Outline each blood parasite and name the species.
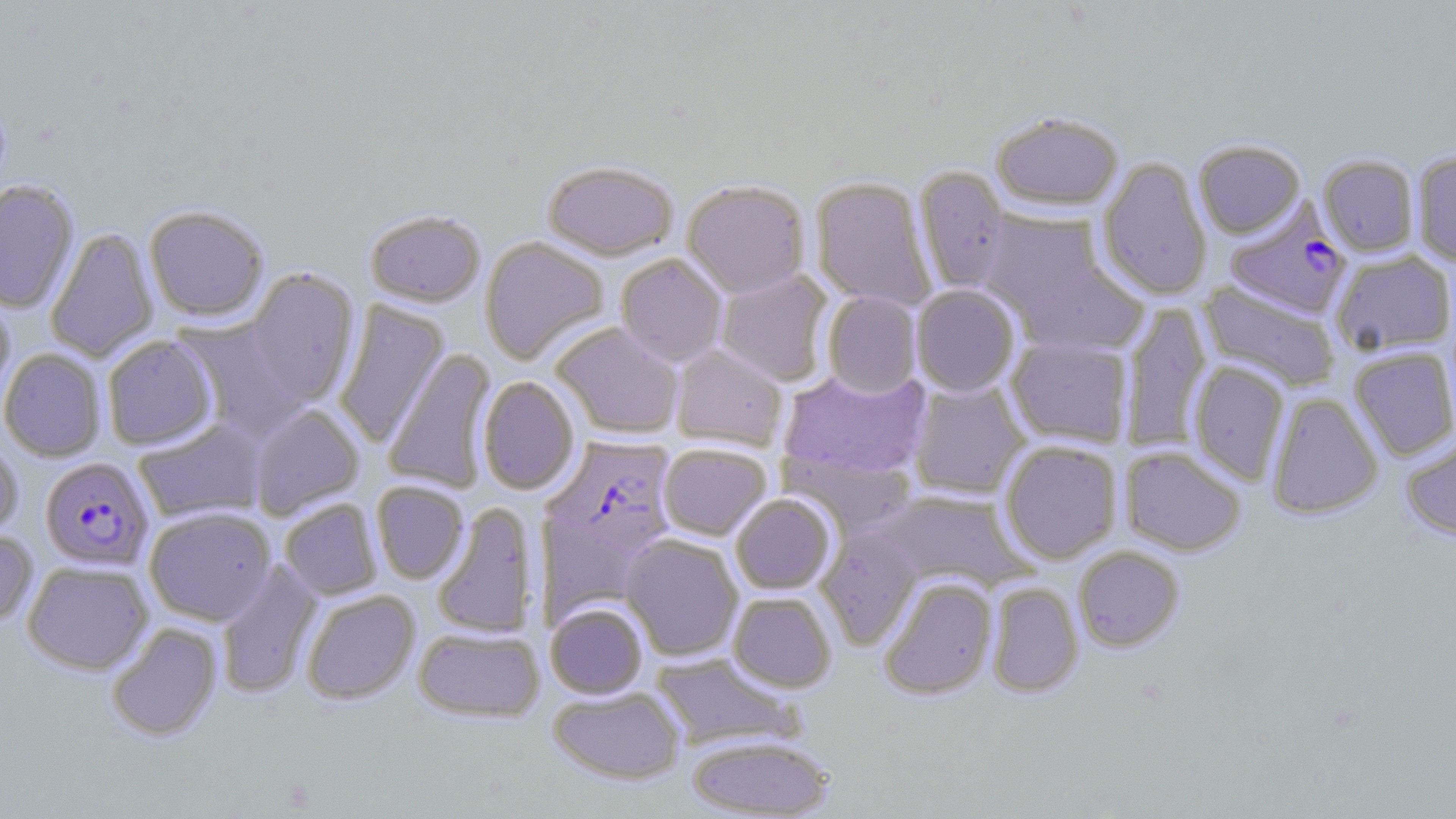
Approximate bounding boxes as [x1, y1, x2, y2] in pixels.
Plasmodium falciparum-infected red blood cells: [1224, 198, 1353, 320], [544, 437, 679, 561], [39, 456, 155, 572].
No Plasmodium ovale, Plasmodium malariae, Plasmodium vivax, Babesia divergens, or Trypanosoma brucei observed.

Uninfected red blood cell locations: [992, 112, 1123, 212], [1194, 140, 1305, 238], [1411, 151, 1456, 266], [1318, 154, 1419, 256], [1098, 156, 1212, 301], [542, 161, 678, 261], [914, 166, 1010, 295], [810, 177, 937, 310], [0, 180, 80, 313], [681, 180, 810, 298], [144, 204, 269, 322], [976, 208, 1105, 318], [364, 209, 485, 308], [45, 226, 159, 363], [479, 236, 609, 366], [1331, 250, 1456, 357], [615, 254, 728, 367], [1015, 260, 1147, 356], [244, 268, 360, 407], [715, 269, 834, 386], [1199, 280, 1341, 392], [911, 285, 1021, 396], [0, 289, 15, 415], [822, 291, 922, 398], [334, 300, 449, 448], [1121, 301, 1211, 452], [174, 319, 306, 443], [550, 322, 684, 439], [102, 335, 218, 450], [1006, 336, 1133, 448], [670, 345, 788, 450], [1349, 346, 1456, 460], [0, 348, 106, 461], [383, 349, 497, 494], [1189, 361, 1290, 485], [778, 367, 931, 480], [478, 376, 580, 496], [908, 381, 1029, 499], [1266, 392, 1383, 519], [250, 403, 364, 520], [133, 418, 267, 524], [0, 435, 23, 543], [1400, 435, 1456, 540], [999, 440, 1122, 563], [658, 443, 772, 540], [1119, 445, 1246, 556], [781, 451, 918, 537], [371, 481, 469, 584], [872, 489, 1035, 591], [730, 493, 836, 595], [279, 498, 382, 600], [431, 502, 538, 640], [144, 507, 276, 625], [815, 526, 922, 649], [0, 530, 38, 627], [620, 533, 743, 661], [1073, 546, 1184, 652], [22, 560, 153, 674], [216, 562, 322, 699], [879, 576, 997, 700], [986, 581, 1083, 699], [301, 590, 420, 705], [728, 592, 836, 692], [545, 602, 648, 699], [106, 622, 222, 743], [413, 627, 545, 723], [651, 653, 802, 751], [547, 685, 685, 785], [686, 734, 835, 818]. Slide-level diagnosis: Plasmodium falciparum. One field of a larger specimen. 1000x magnification. Light microscopy. Thin blood smear. Image is 1456×819 pixels. May-Grünwald-Giemsa-stained preparation.